Report the malaria status of this cell.
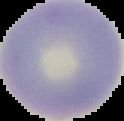

Uninfected.

Summary:
  - Preparation: thin blood film
  - Image type: segmented cell region with the area outside set to black
  - Image size: 124×121 pixels